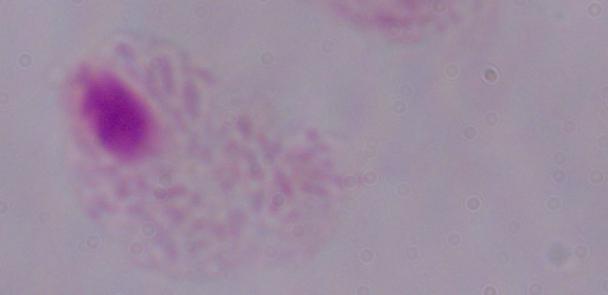 Micrograph. 1000x magnification. A trichomonad is shown.